Locate every leukocyte (white blood cell).
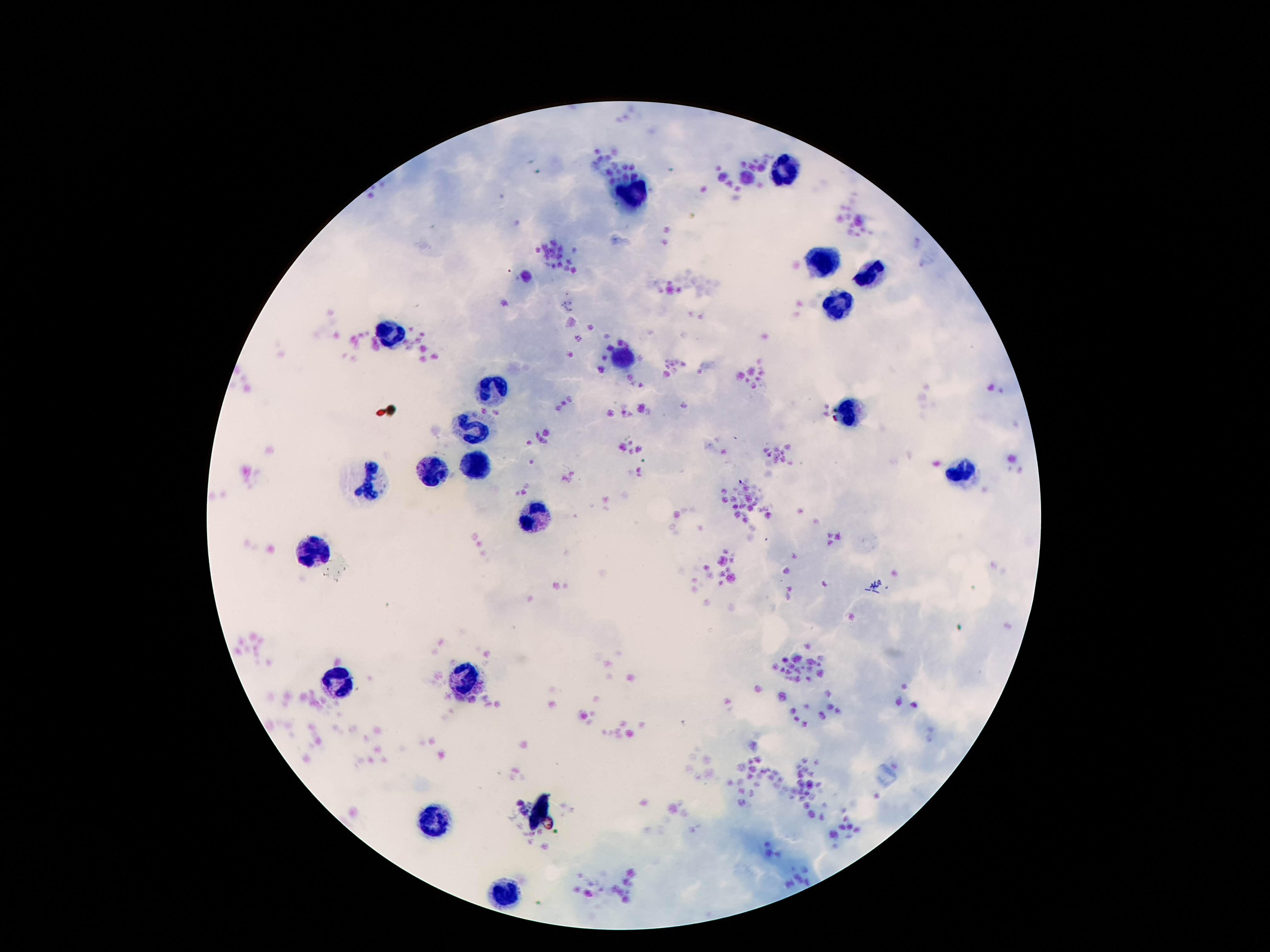
Approximate centers as {x, y} in pixels.
Leukocytes: {785, 169}, {635, 194}, {826, 261}, {873, 273}, {838, 302}, {389, 334}, {627, 354}, {494, 390}, {850, 413}, {473, 425}, {475, 466}, {959, 472}, {432, 474}, {369, 483}, {535, 519}, {314, 552}, {340, 676}, {467, 685}, {438, 821}, {504, 898}.

patient malaria status = negative
field of view = one from this slide
stain = Giemsa
preparation = thick blood smear
capture = smartphone camera through the microscope eyepiece
image size = 1270×952 pixels
magnification = 100x